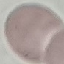

Summary:
  - Malaria status: uninfected
  - Preparation: thin blood film
  - Capture: smartphone through the microscope eyepiece
  - Image type: cell patch, automatically extracted from a larger field of view and resized to 64 × 64 pixels
  - Stain: Giemsa